Outline each blood parasite and name the species.
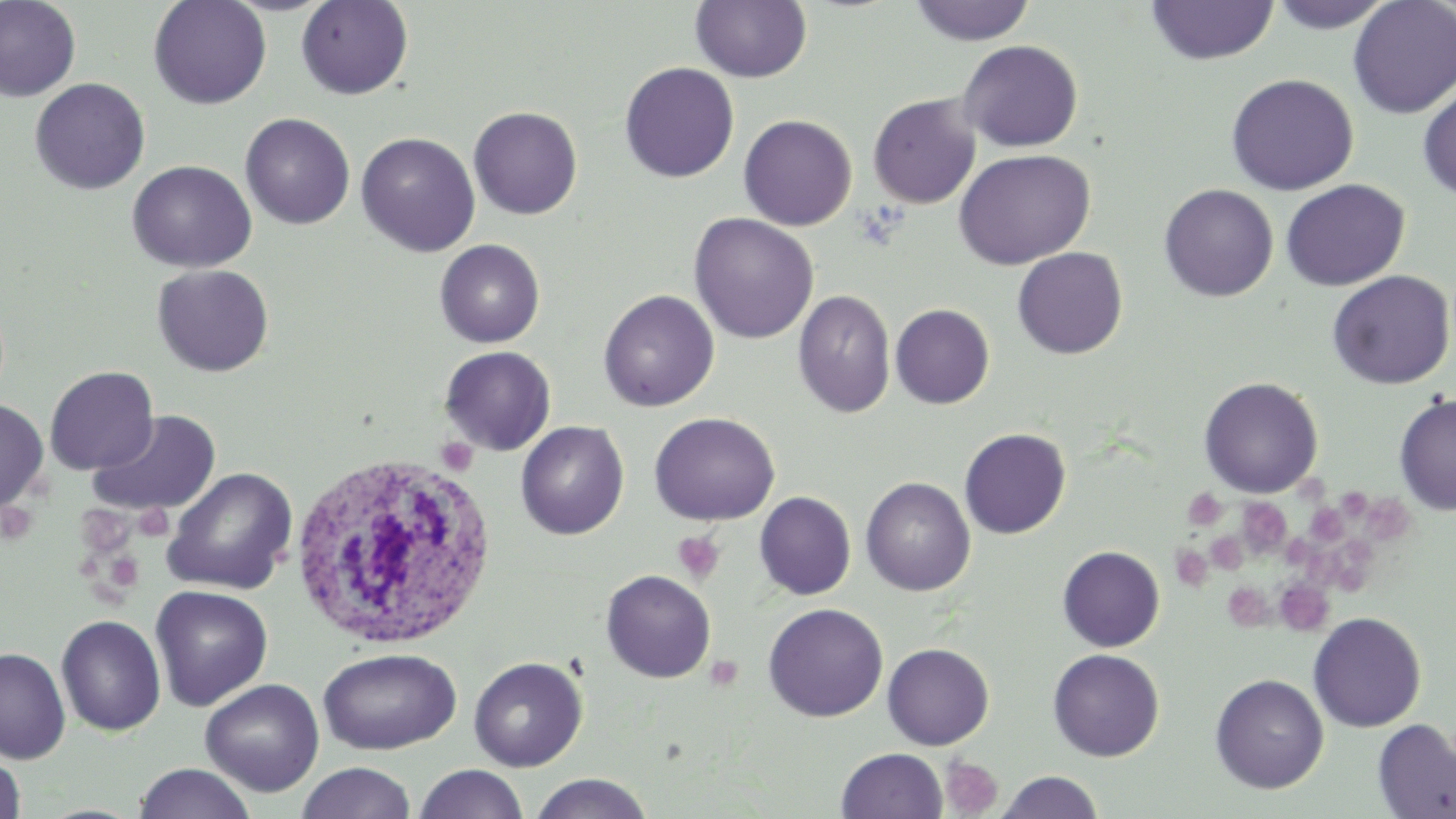

No blood parasites observed.

slide-level diagnosis = no evidence of blood parasites
preparation = thin blood film
stain = May-Grünwald-Giemsa
white blood cell locations = approximate bounding boxes as (x1,y1)-(x2,y2) corner pairs in pixels: (287,451)-(498,651)
field of view = one of a larger specimen
platelet locations = approximate bounding boxes as (x1,y1)-(x2,y2) corner pairs in pixels: (436,437)-(478,476), (1337,487)-(1380,521), (1183,488)-(1227,531), (1365,495)-(1413,554), (1236,496)-(1293,558), (0,502)-(38,545), (134,504)-(173,541), (1305,504)-(1347,545), (75,505)-(136,559), (672,530)-(725,584), (1206,531)-(1247,574), (1280,534)-(1318,569), (1318,536)-(1379,596), (1170,545)-(1213,591), (104,552)-(143,592), (1274,579)-(1334,637), (1222,582)-(1272,629), (704,655)-(744,691), (939,756)-(1003,817)
modality = optical microscopy
uninfected red blood cell locations = approximate bounding boxes as (x1,y1)-(x2,y2) corner pairs in pixels: (0,0)-(81,102), (148,0)-(272,109), (295,0)-(414,100), (1265,0)-(1397,33), (1347,0)-(1456,119), (691,1)-(812,83), (906,1)-(1037,46), (1144,1)-(1280,66), (958,39)-(1083,152), (619,62)-(739,183), (1225,73)-(1359,195), (29,77)-(150,195), (1417,84)-(1456,203), (868,93)-(981,209), (468,106)-(582,219), (240,113)-(355,230), (738,114)-(857,230), (356,132)-(480,256), (953,149)-(1096,270), (127,160)-(257,273), (1280,179)-(1409,291), (1158,184)-(1278,302), (689,213)-(818,344), (434,239)-(545,348), (1012,247)-(1127,359), (151,263)-(275,377), (1327,270)-(1455,390), (598,289)-(720,412), (793,289)-(896,418), (890,304)-(995,409), (440,346)-(556,455), (45,365)-(158,475), (1199,377)-(1323,498), (1394,393)-(1456,517), (0,398)-(48,512), (89,411)-(221,517), (648,412)-(780,525), (515,421)-(629,540), (959,428)-(1071,539), (162,466)-(298,595), (861,477)-(976,596), (754,491)-(856,599), (1057,545)-(1164,652), (601,570)-(716,683), (150,585)-(273,711), (763,603)-(888,722), (1307,611)-(1427,732), (56,614)-(167,736), (882,642)-(994,750), (0,646)-(70,763), (317,647)-(462,754), (1048,648)-(1165,761), (468,656)-(587,771), (1209,673)-(1329,793), (200,679)-(324,796), (1372,718)-(1456,818), (836,748)-(948,819), (0,750)-(27,819), (296,762)-(417,819), (133,763)-(257,819), (415,764)-(529,819), (996,771)-(1104,818), (529,774)-(655,818)
image size = 1456×819 pixels
magnification = 1000x